Point out each malaria parasite.
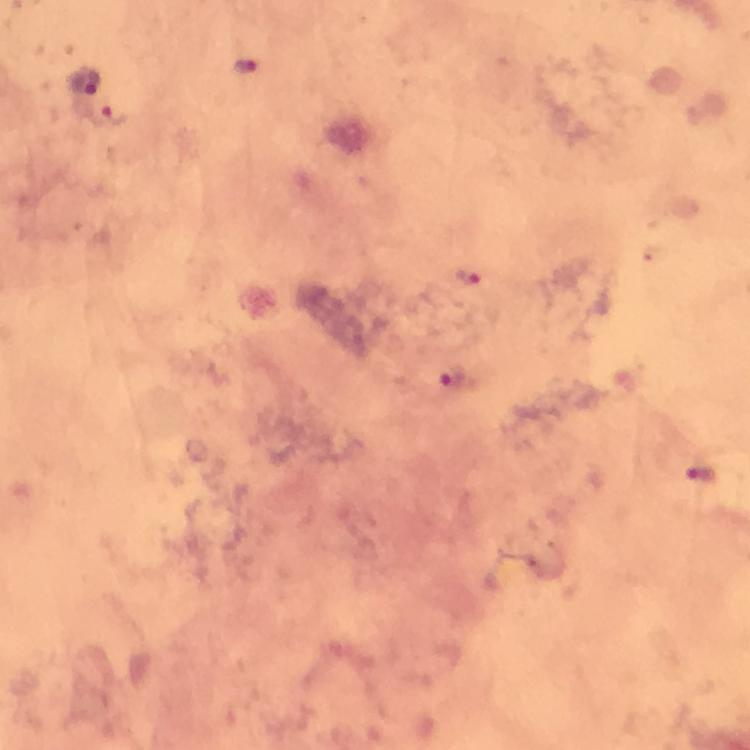

Approximate centers as {x, y} in pixels.
Malaria parasites: {245, 64}, {111, 116}, {468, 276}, {451, 377}, {700, 473}.

Immersion oil was used. From a malaria diagnostic workup. A crop from one field of view. Image is 750×750 pixels. Photographed with a smartphone mounted on the microscope. Thick blood smear. Giemsa-stained preparation. 100x magnification.